Name the parasite shown.
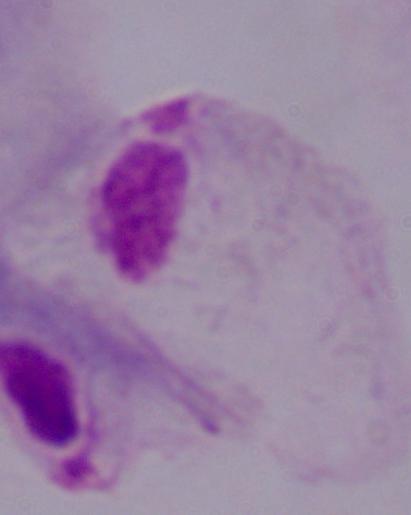
A trichomonad.

magnification = 1000x
modality = photomicrograph